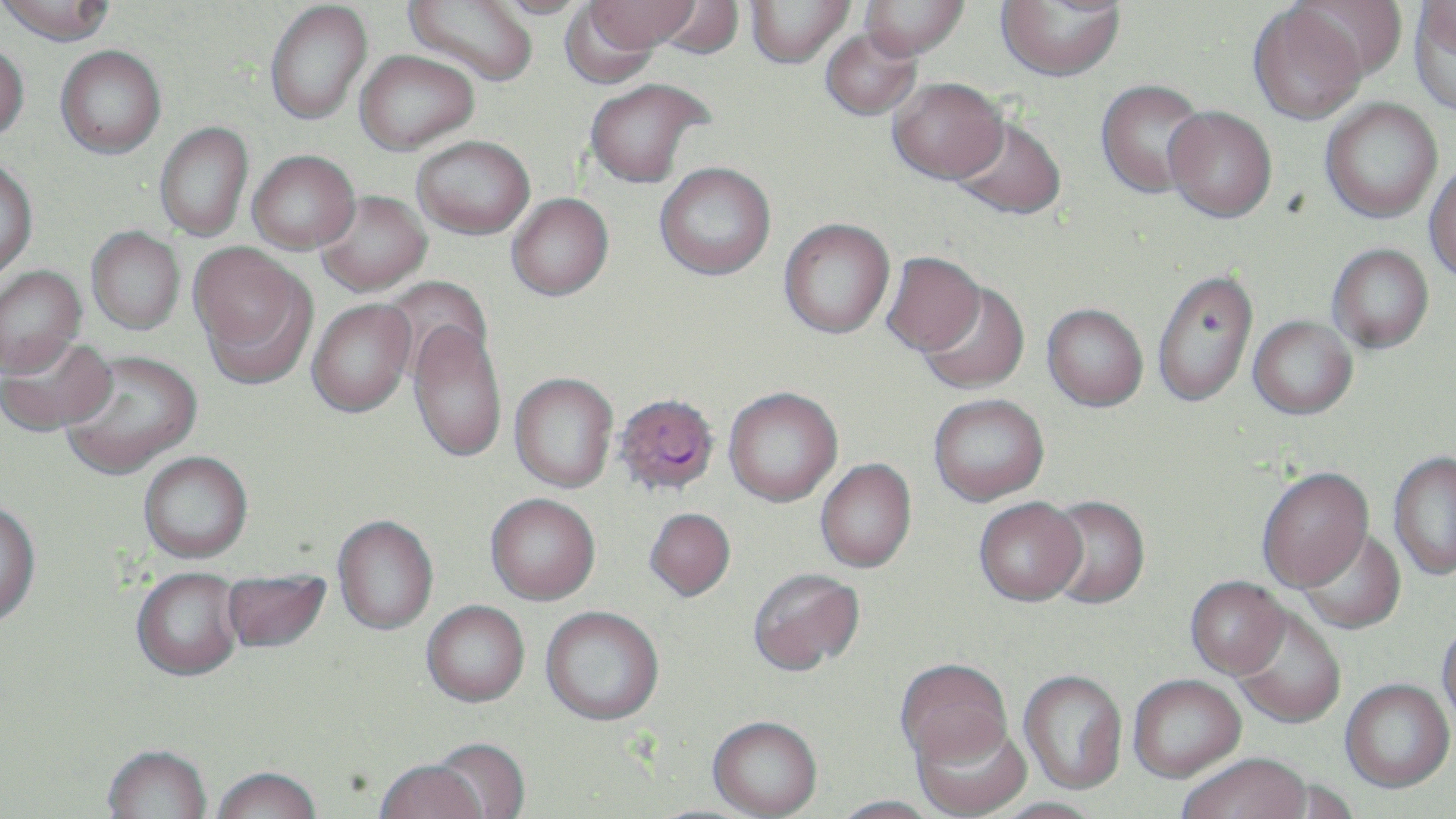

Summary:
  - Coordinate format: approximate bounding boxes as (x1, y1, x2, y2) in pixels
  - Uninfected red blood cell locations: (1, 0, 115, 46), (403, 0, 539, 86), (482, 0, 592, 18), (588, 0, 698, 51), (744, 0, 855, 68), (859, 0, 971, 61), (995, 0, 1125, 80), (1290, 0, 1407, 82), (264, 1, 372, 125), (559, 1, 662, 89), (650, 1, 746, 60), (1410, 1, 1456, 116), (1248, 5, 1367, 125), (820, 27, 922, 120), (0, 41, 29, 142), (55, 46, 166, 158), (354, 50, 479, 153), (584, 77, 713, 188), (888, 77, 1007, 184), (1095, 79, 1209, 197), (1321, 99, 1442, 222), (1163, 106, 1277, 222), (950, 117, 1066, 220), (154, 122, 253, 241), (411, 135, 535, 239), (247, 150, 360, 254), (0, 156, 38, 281), (655, 162, 776, 279), (1424, 165, 1456, 282), (314, 190, 432, 296), (506, 193, 613, 300), (778, 218, 895, 339), (86, 226, 185, 334), (189, 244, 315, 384), (1327, 244, 1433, 353), (881, 251, 986, 355), (0, 266, 86, 377), (1155, 271, 1261, 411), (380, 275, 492, 379), (916, 282, 1030, 397), (307, 299, 416, 419), (1042, 303, 1148, 411), (1248, 316, 1357, 419), (407, 321, 507, 464), (0, 335, 118, 437), (59, 349, 202, 480), (508, 373, 618, 494), (723, 389, 843, 509), (928, 395, 1050, 509), (138, 453, 253, 564), (1389, 453, 1456, 581), (815, 460, 917, 575), (1256, 468, 1373, 593), (485, 496, 601, 608), (1041, 497, 1150, 611), (973, 500, 1087, 609), (0, 501, 41, 630), (645, 511, 736, 604), (333, 517, 438, 637), (1297, 528, 1405, 635), (222, 569, 332, 656), (131, 570, 243, 685), (747, 570, 865, 679), (1185, 579, 1290, 681), (422, 603, 530, 709), (540, 608, 664, 728), (1231, 609, 1345, 730), (1436, 622, 1456, 732), (896, 661, 1012, 773), (1019, 672, 1127, 796), (1129, 677, 1246, 784), (1340, 681, 1455, 795), (707, 719, 822, 819), (912, 720, 1032, 819), (430, 740, 530, 818), (102, 748, 212, 819), (1179, 757, 1311, 819), (373, 762, 486, 819), (211, 770, 322, 819), (1259, 776, 1361, 819), (831, 798, 942, 819), (989, 799, 1103, 819)
  - Plasmodium falciparum-infected red blood cell locations: (614, 394, 720, 498)
  - Slide-level diagnosis: Plasmodium falciparum
  - Magnification: 1000x
  - Modality: light microscopy
  - Preparation: thin blood smear
  - Field of view: single
  - Stain: May-Grünwald-Giemsa
  - Image size: 1456×819 pixels